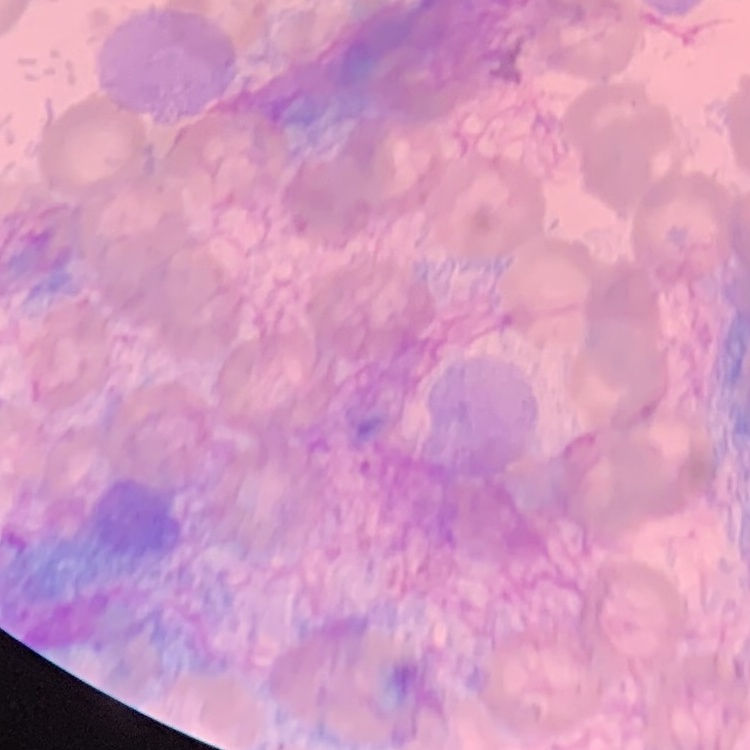
The red blood cells show no rouleaux formation. Thin peripheral smear. Field's or Giemsa stain. Square crop of a larger photomicrograph.